Name the blood parasite species.
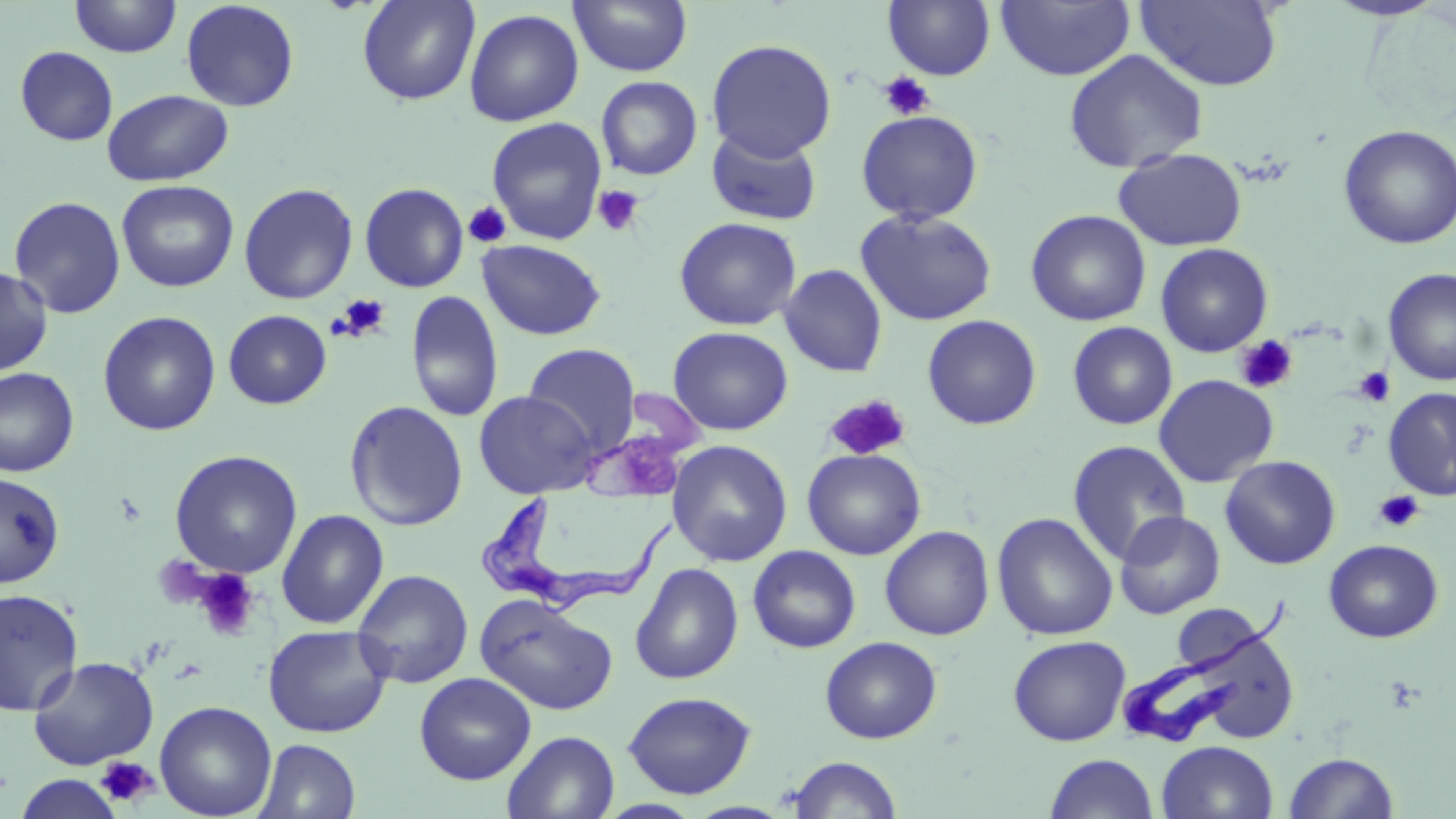

Trypanosoma brucei.

Approximate bounding boxes as [x1, y1, x2, y2] in pixels. Platelet locations: [880, 71, 935, 121], [593, 184, 644, 237], [464, 202, 511, 248], [334, 294, 391, 341], [1234, 335, 1297, 394], [1353, 367, 1396, 407], [823, 395, 911, 462], [1373, 490, 1425, 533], [191, 567, 262, 641], [95, 756, 159, 809]. Uninfected red blood cell locations: [69, 0, 182, 58], [180, 0, 300, 112], [357, 0, 480, 106], [568, 0, 693, 77], [1135, 0, 1284, 91], [1321, 0, 1452, 22], [883, 1, 996, 81], [996, 1, 1134, 81], [464, 8, 584, 127], [706, 39, 837, 162], [14, 45, 118, 146], [1064, 49, 1207, 173], [595, 75, 703, 181], [102, 88, 234, 187], [856, 110, 983, 225], [486, 117, 607, 245], [706, 125, 822, 226], [1338, 125, 1456, 249], [1113, 148, 1247, 251], [116, 180, 239, 292], [360, 182, 469, 292], [238, 183, 359, 305], [8, 195, 127, 319], [856, 209, 997, 326], [1026, 209, 1151, 326], [674, 216, 802, 331], [476, 239, 607, 340], [1155, 243, 1273, 357], [778, 264, 888, 377], [0, 265, 53, 377], [1382, 267, 1456, 386], [406, 290, 505, 423], [223, 310, 332, 409], [98, 311, 221, 436], [922, 315, 1042, 430], [1067, 322, 1177, 430], [667, 326, 793, 435], [523, 343, 641, 455], [0, 367, 80, 478], [1154, 374, 1279, 487], [1383, 387, 1456, 501], [474, 390, 598, 499], [344, 400, 469, 531], [667, 439, 793, 567], [1066, 439, 1191, 565], [802, 448, 926, 560], [169, 449, 303, 579], [1220, 455, 1341, 569], [0, 471, 65, 588], [276, 509, 389, 629], [1114, 510, 1225, 619], [992, 512, 1118, 641], [880, 525, 995, 640], [1322, 539, 1444, 642], [747, 545, 861, 653], [630, 563, 744, 685], [352, 569, 474, 689], [0, 588, 83, 716], [475, 594, 618, 716], [1179, 602, 1296, 744], [262, 624, 394, 738], [1008, 634, 1131, 746], [820, 636, 942, 744], [27, 655, 159, 770], [414, 671, 536, 785], [622, 690, 757, 799], [154, 699, 277, 819], [502, 730, 620, 818], [254, 738, 361, 819], [1156, 740, 1279, 819], [1284, 751, 1400, 818], [1044, 752, 1160, 818], [786, 755, 903, 818], [14, 772, 125, 819]. Trypanosoma brucei locations: [476, 495, 681, 622], [1123, 594, 1299, 750]. One field of a larger specimen. Image is 1456×819 pixels. 1000x magnification. Light microscopy. May-Grünwald-Giemsa-stained preparation. Thin blood film.